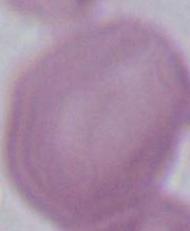
Summary:
  - Identification: erythrocyte
  - Modality: micrograph
  - Magnification: 1000x